Locate every blood parasite and identify its species.
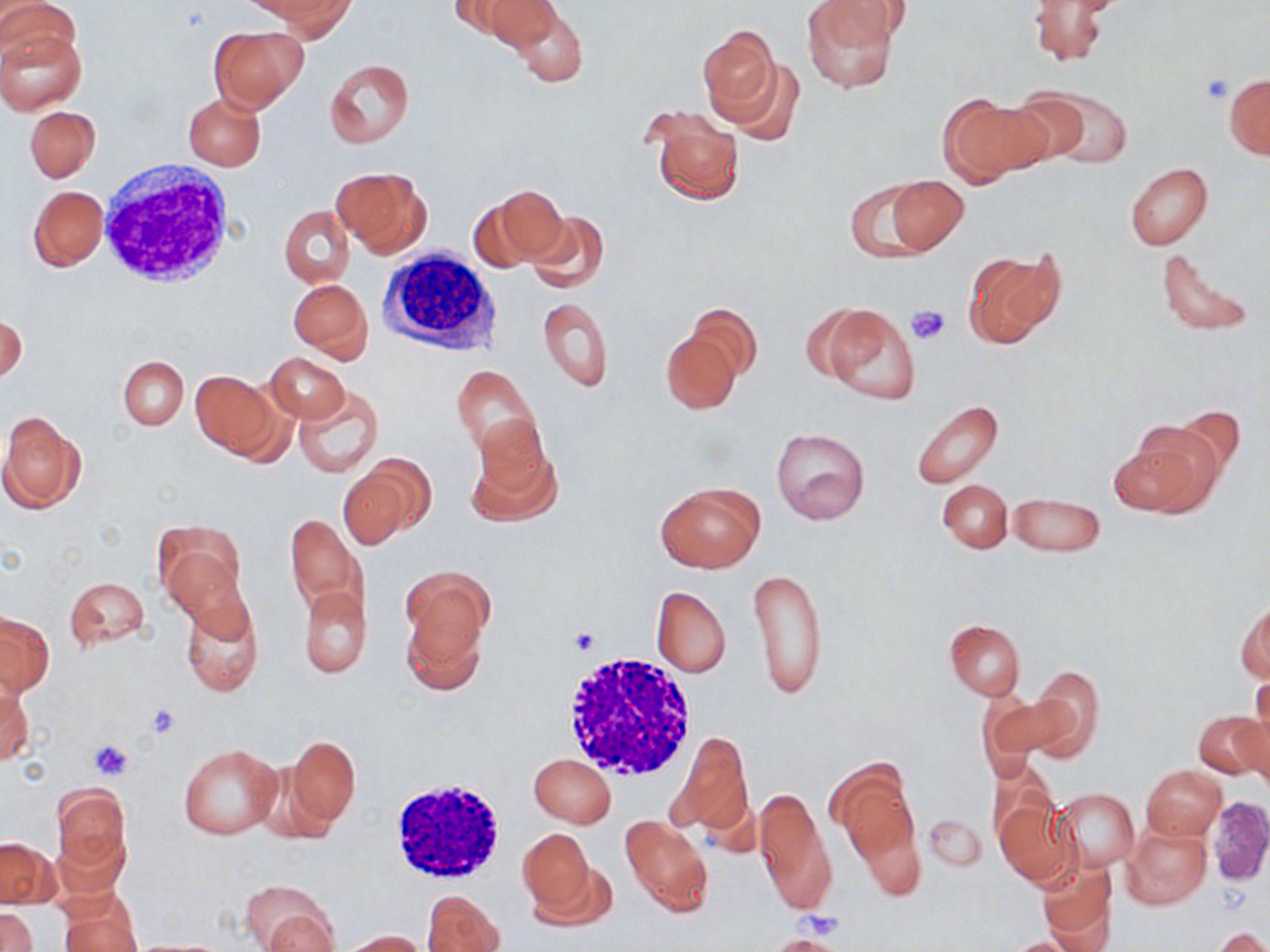

No blood parasites observed.

{
  "slide_level_diagnosis": "no evidence of blood parasites",
  "field_of_view": "single",
  "uninfected_red_blood_cell_locations": "approximate bounding boxes as (x1, y1, x2, y2) in pixels: (1, 0, 80, 71), (448, 0, 535, 44), (481, 0, 560, 50), (801, 0, 900, 93), (818, 0, 913, 46), (1027, 0, 1113, 66), (262, 1, 355, 38), (509, 6, 587, 89), (209, 26, 306, 113), (698, 26, 783, 124), (0, 29, 86, 114), (711, 53, 803, 142), (324, 59, 414, 148), (1224, 73, 1269, 160), (1040, 89, 1134, 168), (183, 92, 266, 171), (986, 93, 1085, 172), (937, 94, 1046, 185), (25, 105, 100, 183), (644, 105, 745, 208), (1125, 163, 1214, 251), (332, 166, 431, 258), (882, 175, 968, 255), (843, 179, 939, 262), (28, 184, 107, 271), (482, 185, 568, 267), (278, 204, 354, 287), (525, 210, 609, 291), (1154, 246, 1256, 337), (963, 248, 1063, 351), (288, 277, 373, 361), (537, 296, 614, 391), (685, 303, 761, 380), (813, 304, 921, 408), (1, 314, 26, 382), (661, 332, 741, 414), (265, 351, 349, 422), (119, 356, 188, 429), (451, 365, 541, 458), (190, 371, 279, 457), (292, 384, 383, 478), (911, 399, 1005, 489), (0, 410, 87, 515), (467, 421, 562, 526), (1111, 424, 1221, 518), (770, 428, 870, 526), (344, 455, 435, 542), (938, 479, 1013, 553), (655, 481, 763, 573), (1008, 492, 1105, 557), (285, 513, 368, 618), (154, 522, 246, 619), (748, 564, 828, 701), (402, 570, 491, 669), (63, 576, 151, 652), (298, 585, 371, 678), (651, 586, 732, 678), (179, 593, 263, 698), (1239, 598, 1269, 682), (1, 611, 55, 696), (944, 620, 1027, 699), (1024, 666, 1105, 760), (1, 680, 32, 767), (1246, 682, 1269, 763), (977, 690, 1063, 773), (1194, 710, 1268, 782), (1236, 714, 1270, 797), (669, 732, 754, 836), (286, 735, 360, 830), (178, 744, 282, 839), (529, 754, 616, 826), (827, 760, 919, 870), (1141, 766, 1225, 839), (51, 781, 133, 884), (755, 786, 834, 916), (1052, 788, 1137, 872), (1205, 796, 1270, 885), (994, 801, 1075, 885), (922, 812, 987, 872), (619, 815, 713, 918), (1121, 824, 1211, 909), (518, 829, 598, 921), (0, 837, 59, 908), (1037, 860, 1116, 946), (242, 879, 340, 951), (422, 889, 504, 952), (58, 893, 141, 952), (0, 907, 39, 952), (1208, 925, 1270, 951), (341, 929, 427, 952), (768, 935, 847, 952), (1001, 936, 1090, 952)",
  "platelet_locations": "approximate bounding boxes as (x1, y1, x2, y2) in pixels: (1201, 74, 1234, 102), (907, 303, 951, 347), (567, 626, 601, 655), (146, 703, 183, 740), (88, 738, 132, 779)",
  "modality": "light microscopy",
  "image_size": "1270×952 pixels",
  "magnification": "1000x",
  "white_blood_cell_locations": "approximate bounding boxes as (x1, y1, x2, y2) in pixels: (95, 163, 237, 289), (377, 247, 503, 353), (561, 651, 702, 781), (387, 778, 507, 886)",
  "preparation": "thin blood smear",
  "stain": "May-Grünwald-Giemsa"
}